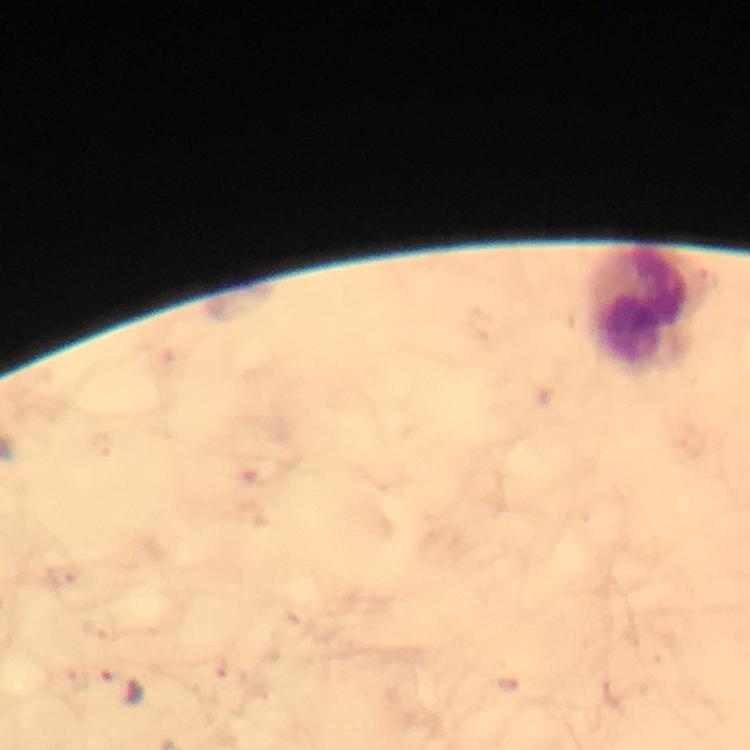
Approximate centers as (x, y) in pixels.
Summary:
  - Leukocyte locations: (641, 311)
  - Malaria parasite locations: (120, 688)
  - Capture: smartphone photograph through a microscope
  - Magnification: 100x
  - Image size: 750×750 pixels
  - Cropped from: a single field of view
  - Preparation: thick blood film
  - Stain: Giemsa
  - Context: from a diagnostic examination for malaria
  - Immersion oil: used